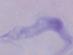 Captured at 1000x magnification. Micrograph. A trypanosome is shown.